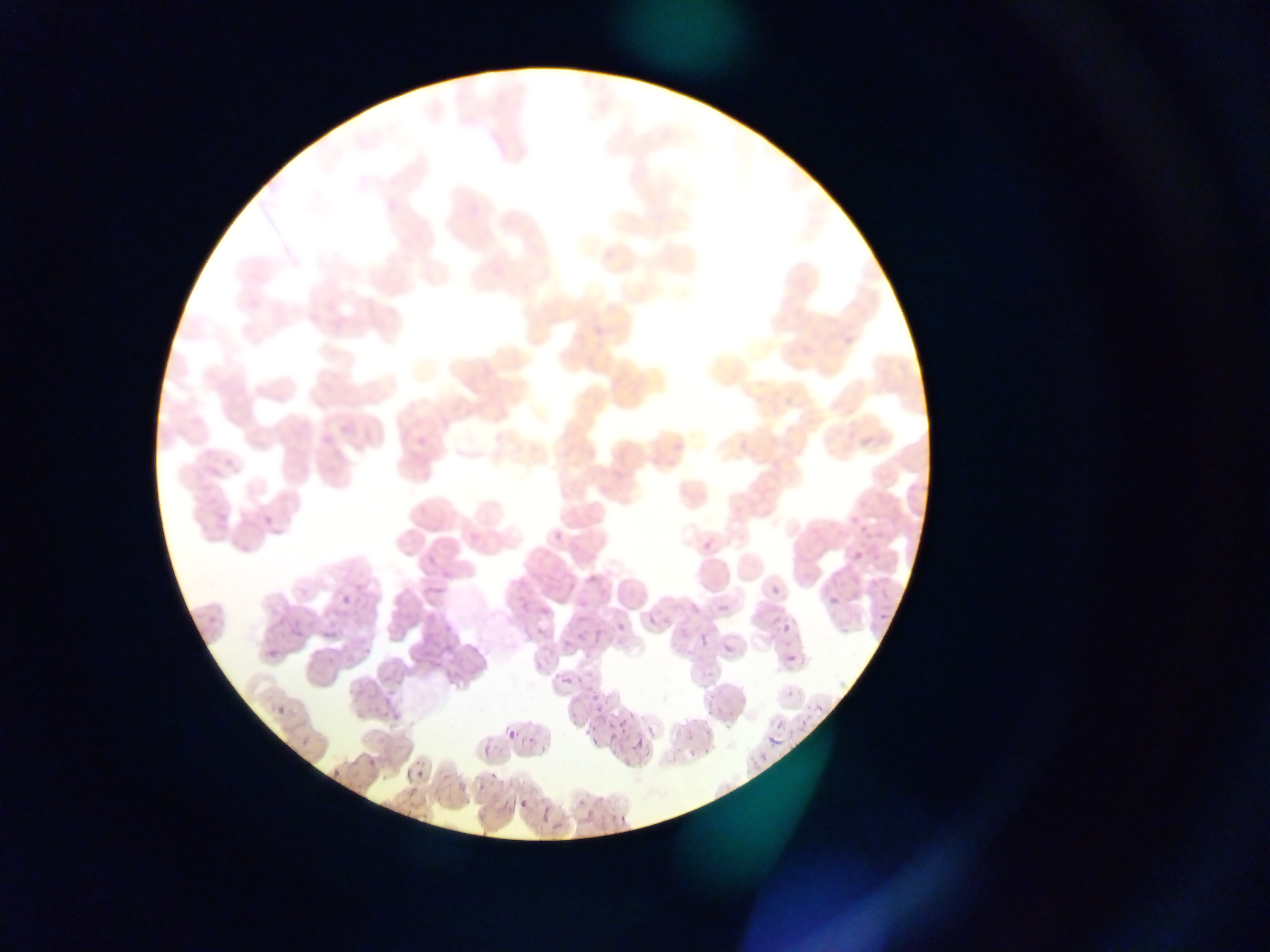

Approximate bounding boxes as {left, top, right, bottom} in pixels.
Summary:
  - Plasmodium parasite locations: {768, 583, 782, 598}, {536, 603, 553, 620}, {778, 619, 794, 636}, {294, 620, 309, 635}, {614, 620, 628, 635}, {723, 639, 738, 658}, {784, 652, 800, 667}, {813, 702, 827, 717}, {764, 727, 786, 749}, {507, 728, 519, 742}, {409, 763, 429, 785}, {517, 797, 530, 812}
  - Field of view: single
  - Country: Ghana
  - Image size: 1270×952 pixels
  - Capture: mobile-phone photograph through a microscope
  - Preparation: thin blood smear